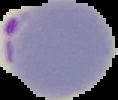 Malaria status: parasitized. Image is 118×100 pixels. Segmented cell region on a black background. From a thin blood smear.